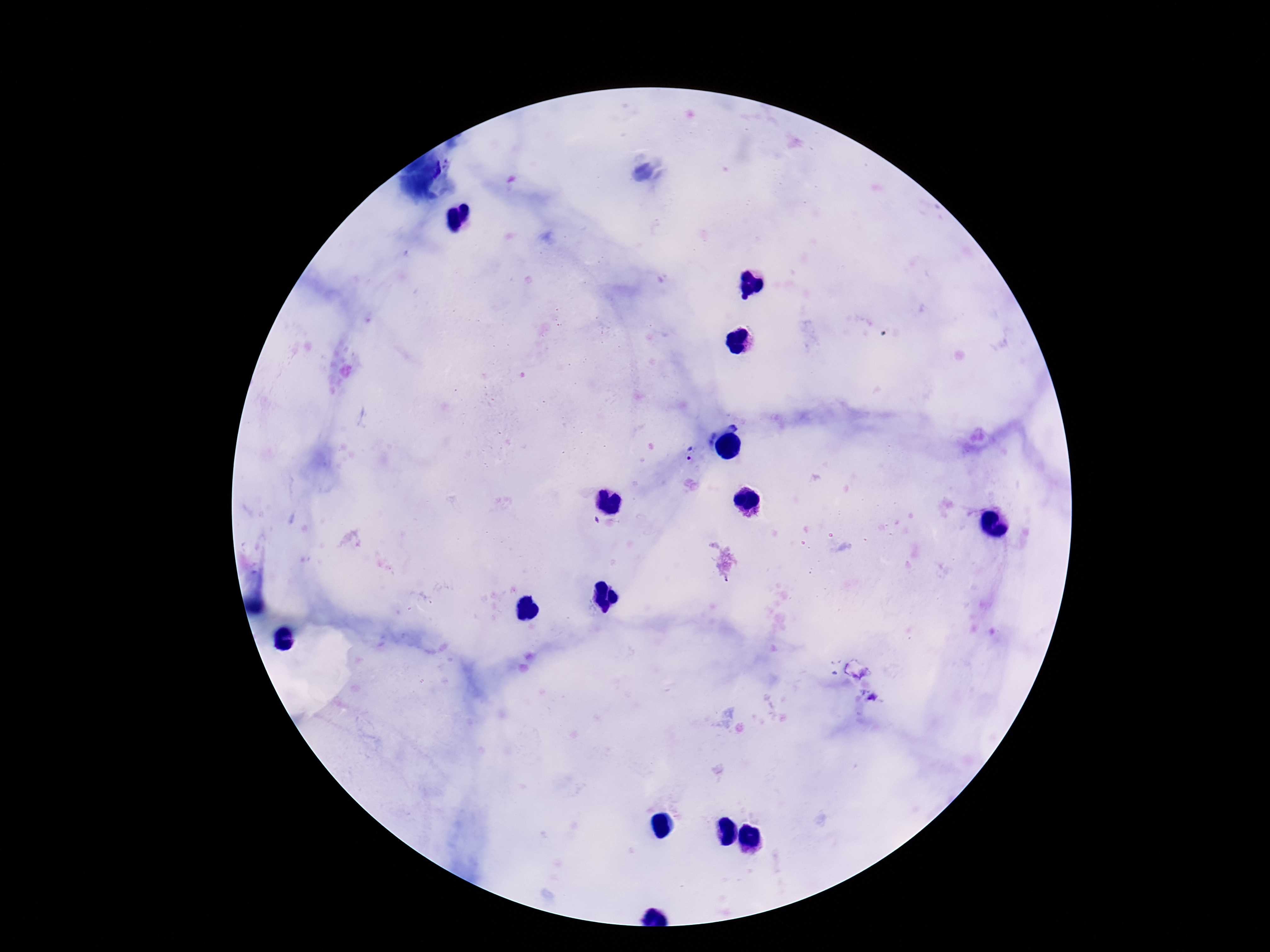
field_of_view: single
image_size: 1270×952 pixels
preparation: thick blood smear
capture: smartphone camera through the microscope eyepiece
patient_malaria_status: positive
stain: Giemsa
magnification: 100x
plasmodium_parasite_locations: 'approximate centers as [x, y] in pixels: [687, 454], [872, 698]'